Assess this cell for malaria.
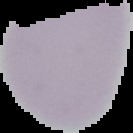

Uninfected.

From a thin blood film. Image is 133×133 pixels. Segmented cell region on a black background.